Name the parasite shown.
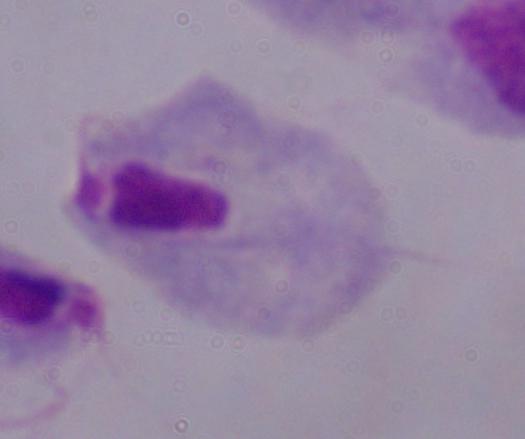
A trichomonad.

Photomicrograph. Captured at 1000x magnification.